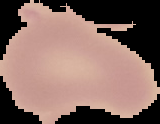

Summary:
  - Image type: segmented cell region on a black background
  - Image size: 160×124 pixels
  - Preparation: thin blood film
  - Malaria status: uninfected